Give the extent of all Plasmodium falciparum-infected red blood cells.
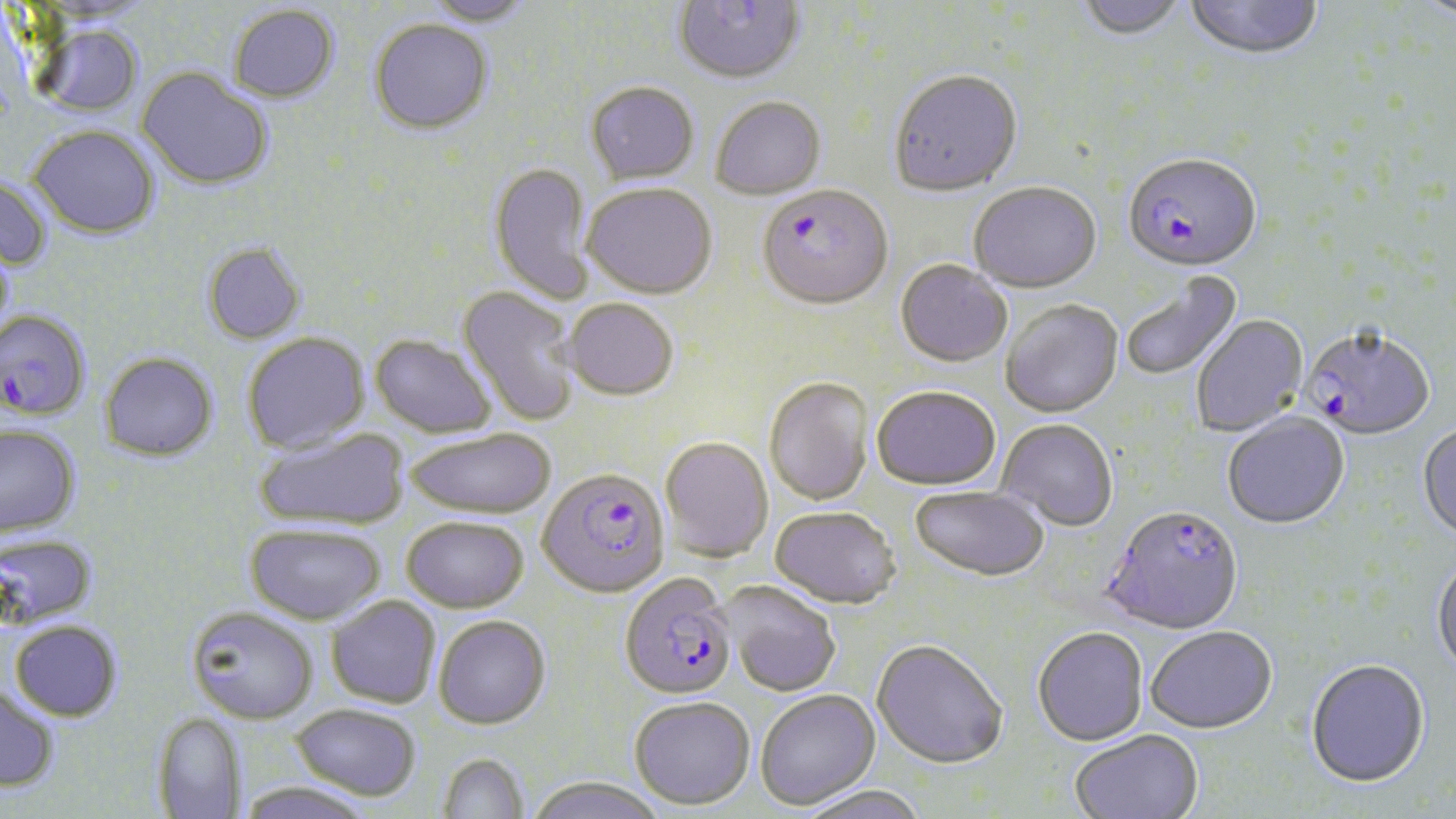

Approximate bounding boxes as (x1, y1, x2, y2) in pixels.
Plasmodium falciparum-infected red blood cells: (1122, 156, 1262, 275), (757, 187, 892, 312), (0, 308, 92, 422), (1301, 330, 1435, 442), (538, 468, 671, 598), (1105, 508, 1244, 637), (620, 573, 738, 699).

Uninfected red blood cell locations: (420, 0, 534, 27), (673, 0, 806, 86), (1075, 0, 1189, 44), (1184, 0, 1324, 63), (1417, 0, 1456, 28), (228, 4, 340, 103), (369, 19, 494, 136), (30, 24, 145, 119), (136, 67, 273, 191), (888, 71, 1023, 199), (585, 82, 699, 185), (711, 97, 826, 201), (28, 126, 160, 239), (488, 162, 595, 304), (0, 174, 52, 273), (582, 183, 717, 299), (968, 184, 1102, 296), (0, 236, 16, 347), (201, 242, 307, 345), (895, 260, 1012, 368), (1120, 271, 1243, 382), (457, 286, 582, 427), (563, 298, 678, 401), (1000, 301, 1124, 420), (1191, 316, 1308, 437), (241, 332, 371, 454), (369, 334, 497, 438), (100, 352, 218, 462), (764, 378, 874, 506), (872, 386, 1000, 491), (1222, 413, 1350, 531), (995, 419, 1118, 532), (0, 424, 81, 536), (1417, 424, 1456, 545), (253, 427, 410, 531), (406, 427, 556, 518), (659, 436, 774, 562), (910, 487, 1049, 582), (769, 507, 901, 609), (401, 516, 529, 612), (246, 522, 386, 624), (0, 532, 97, 629), (1431, 558, 1456, 679), (719, 581, 841, 697), (326, 596, 441, 708), (186, 606, 319, 724), (434, 615, 551, 729), (10, 620, 122, 721), (1032, 628, 1148, 748), (1147, 629, 1277, 736), (871, 641, 1008, 771), (1306, 661, 1430, 791), (0, 685, 60, 791), (755, 689, 880, 809), (629, 696, 755, 809), (291, 703, 423, 800), (151, 712, 248, 818), (1070, 731, 1203, 819), (436, 752, 530, 818), (525, 776, 667, 819), (235, 780, 377, 819), (795, 784, 930, 819). Slide-level diagnosis: Plasmodium falciparum. 1000x magnification. Thin blood smear. May-Grünwald-Giemsa-stained preparation. Single field of view. Light microscopy. Image is 1456×819 pixels.